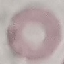

Result: no malaria parasites detected. Giemsa-stained preparation. Thin blood smear. Automatically extracted cell patch, resized to 64 × 64 pixels. Photographed with a smartphone camera at the microscope eyepiece.